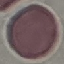

malaria status = uninfected
capture = smartphone through the microscope eyepiece
image type = cell patch, automatically extracted from a larger field of view and resized to 64 × 64 pixels
stain = Giemsa
preparation = thin blood film